Locate and identify every blood parasite.
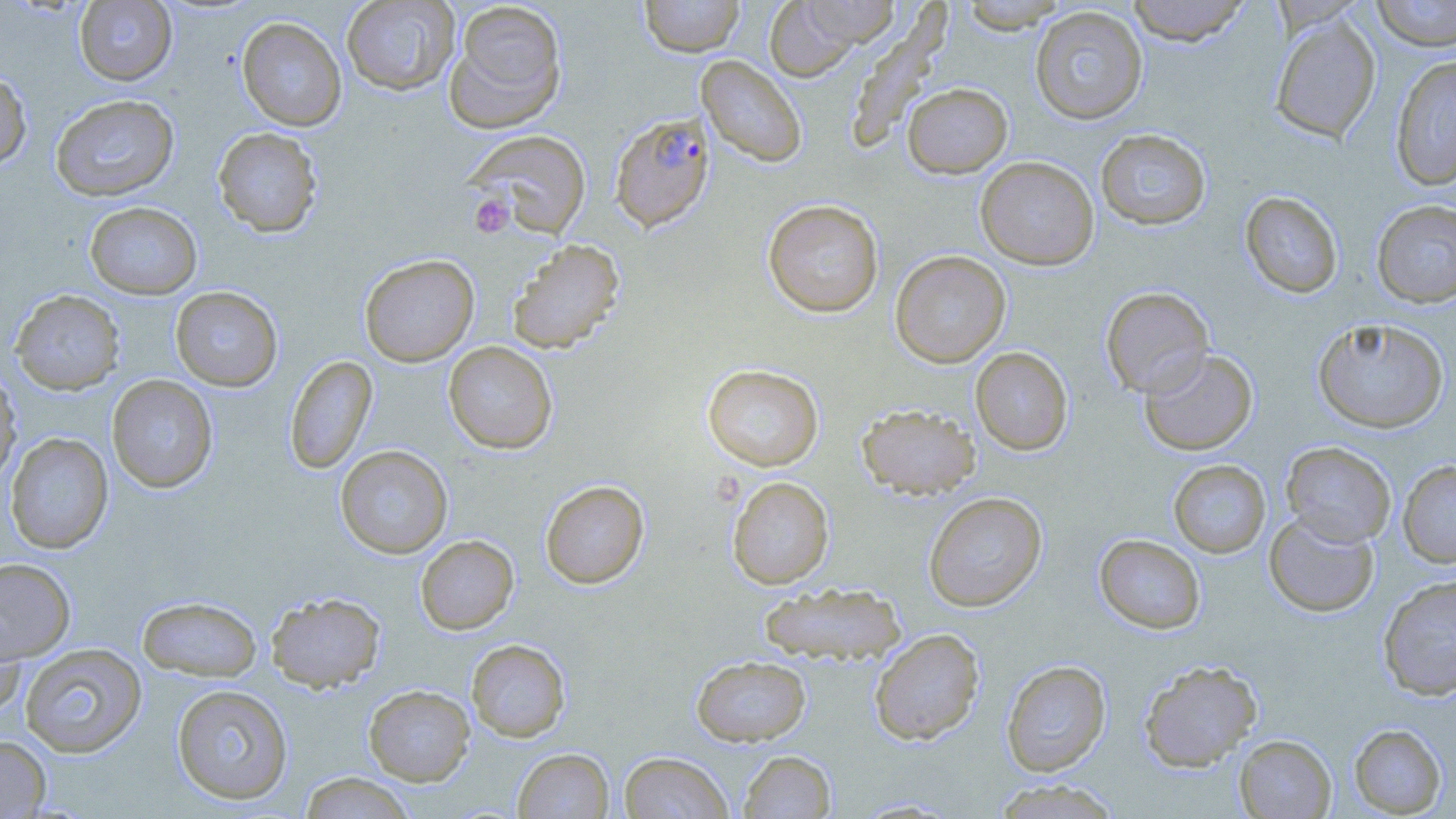

Approximate bounding boxes as [x1, y1, x2, y2] in pixels.
Plasmodium falciparum-infected red blood cells: [609, 112, 715, 232].
No Plasmodium ovale, Plasmodium malariae, Plasmodium vivax, Babesia divergens, or Trypanosoma brucei observed.

Uninfected red blood cell locations: [341, 0, 460, 96], [638, 0, 745, 58], [1125, 0, 1251, 46], [1370, 0, 1456, 51], [74, 1, 177, 86], [444, 1, 568, 133], [762, 1, 870, 81], [956, 1, 1071, 33], [1030, 6, 1148, 124], [1269, 14, 1381, 144], [237, 16, 347, 131], [696, 55, 807, 168], [1390, 55, 1456, 191], [0, 70, 33, 170], [902, 83, 1012, 178], [50, 94, 180, 201], [212, 127, 323, 237], [1095, 128, 1211, 230], [464, 129, 592, 238], [975, 156, 1099, 270], [1240, 191, 1343, 298], [762, 199, 884, 317], [1371, 199, 1456, 308], [84, 201, 203, 300], [507, 239, 625, 354], [890, 251, 1011, 367], [359, 253, 479, 367], [170, 286, 283, 392], [1100, 286, 1214, 398], [10, 289, 125, 394], [1312, 317, 1449, 434], [443, 341, 558, 454], [970, 347, 1073, 455], [1139, 348, 1258, 456], [284, 355, 378, 475], [702, 364, 824, 471], [0, 369, 21, 487], [106, 375, 219, 493], [855, 403, 981, 499], [5, 432, 114, 554], [1281, 442, 1396, 547], [335, 445, 453, 559], [1168, 459, 1271, 558], [1398, 460, 1456, 568], [726, 476, 834, 589], [540, 480, 650, 589], [923, 491, 1047, 612], [1264, 512, 1379, 617], [1094, 534, 1206, 634], [415, 535, 519, 634], [0, 558, 76, 663], [1377, 575, 1456, 700], [758, 581, 907, 667], [266, 591, 385, 692], [137, 595, 263, 681], [0, 612, 26, 721], [869, 628, 985, 745], [466, 639, 571, 742], [20, 643, 147, 758], [691, 654, 811, 746], [1138, 659, 1262, 771], [1001, 660, 1112, 777], [171, 683, 294, 805], [363, 685, 475, 785], [1349, 723, 1447, 817], [0, 734, 51, 817], [1234, 734, 1336, 818], [513, 748, 614, 819], [738, 750, 836, 818], [619, 752, 733, 818], [298, 772, 417, 819], [990, 779, 1124, 818]. Platelet locations: [470, 194, 514, 237]. Slide-level diagnosis: Plasmodium falciparum. Image is 1456×819 pixels. Captured at 1000x magnification. Single field of view. May-Grünwald-Giemsa-stained preparation. Optical microscopy. Thin blood smear.